Comment on the morphology of the erythrocytes.
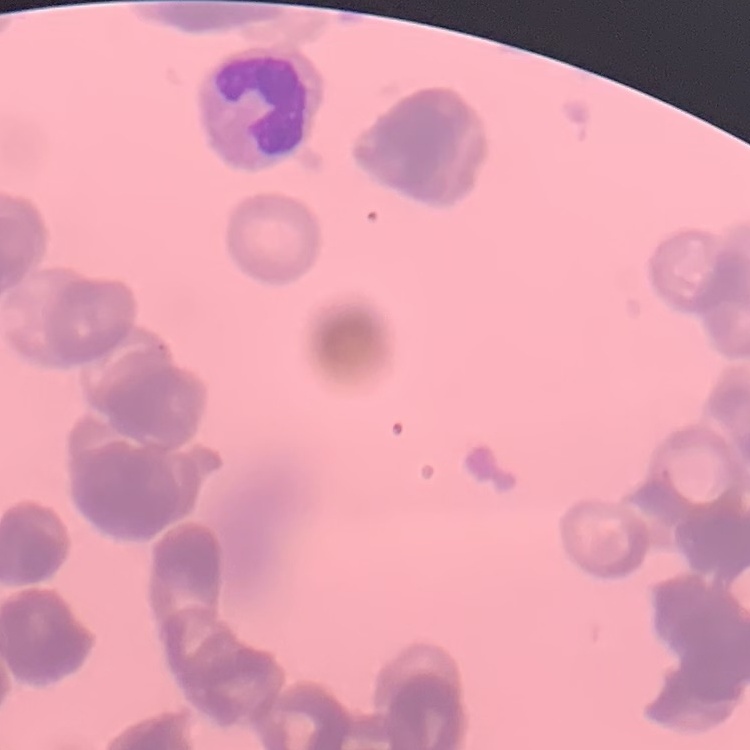

They show rouleaux formation.

Summary:
  - Stain: Field's or Giemsa
  - Image type: square crop of a larger photomicrograph
  - Preparation: thin blood smear